Classify this cell by malaria status.
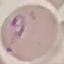

Parasitized.

Thin smear of blood. Automatically extracted cell patch, resized to 64 × 64 pixels. Acquired by smartphone through the microscope eyepiece. Giemsa stain.